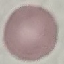

malaria status = uninfected
preparation = thin blood smear
capture = smartphone camera at the microscope eyepiece
stain = Giemsa
image type = cell patch, automatically extracted from a larger field of view and resized to 64 × 64 pixels